Name the parasite shown.
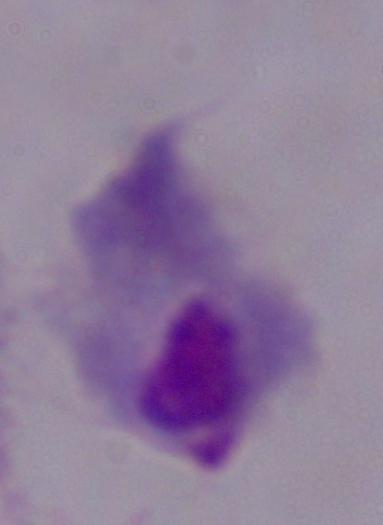

This is a trichomonad.

magnification: 1000x
modality: micrograph